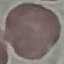

Summary:
  - Malaria status: uninfected
  - Preparation: thin blood film
  - Stain: Giemsa
  - Capture: smartphone camera at the microscope eyepiece
  - Image type: automatically extracted cell patch, resized to 64 × 64 pixels